Point out each Plasmodium parasite.
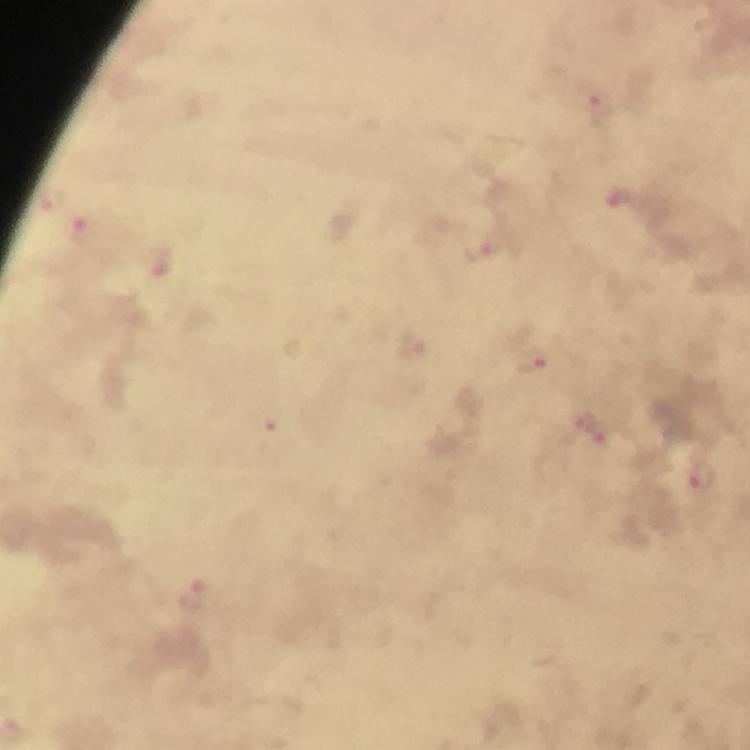
Approximate object centers, in pixels from the top-left corner.
Plasmodium parasites: (x=596, y=103), (x=619, y=197), (x=80, y=229), (x=483, y=247), (x=157, y=262), (x=412, y=344), (x=530, y=362), (x=271, y=426), (x=592, y=430), (x=703, y=482), (x=192, y=597).

cropped from = a single field of view
immersion oil = used
capture = smartphone mounted on the microscope
context = from a diagnostic examination for malaria
image size = 750×750 pixels
stain = Giemsa
preparation = thick blood film
magnification = 100x